Report the malaria status of this cell.
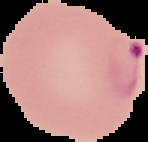
Parasitized.

Summary:
  - Image type: segmented cell region with the area outside set to black
  - Image size: 148×142 pixels
  - Preparation: thin blood smear